Give the extent of all uninfected red blood cells.
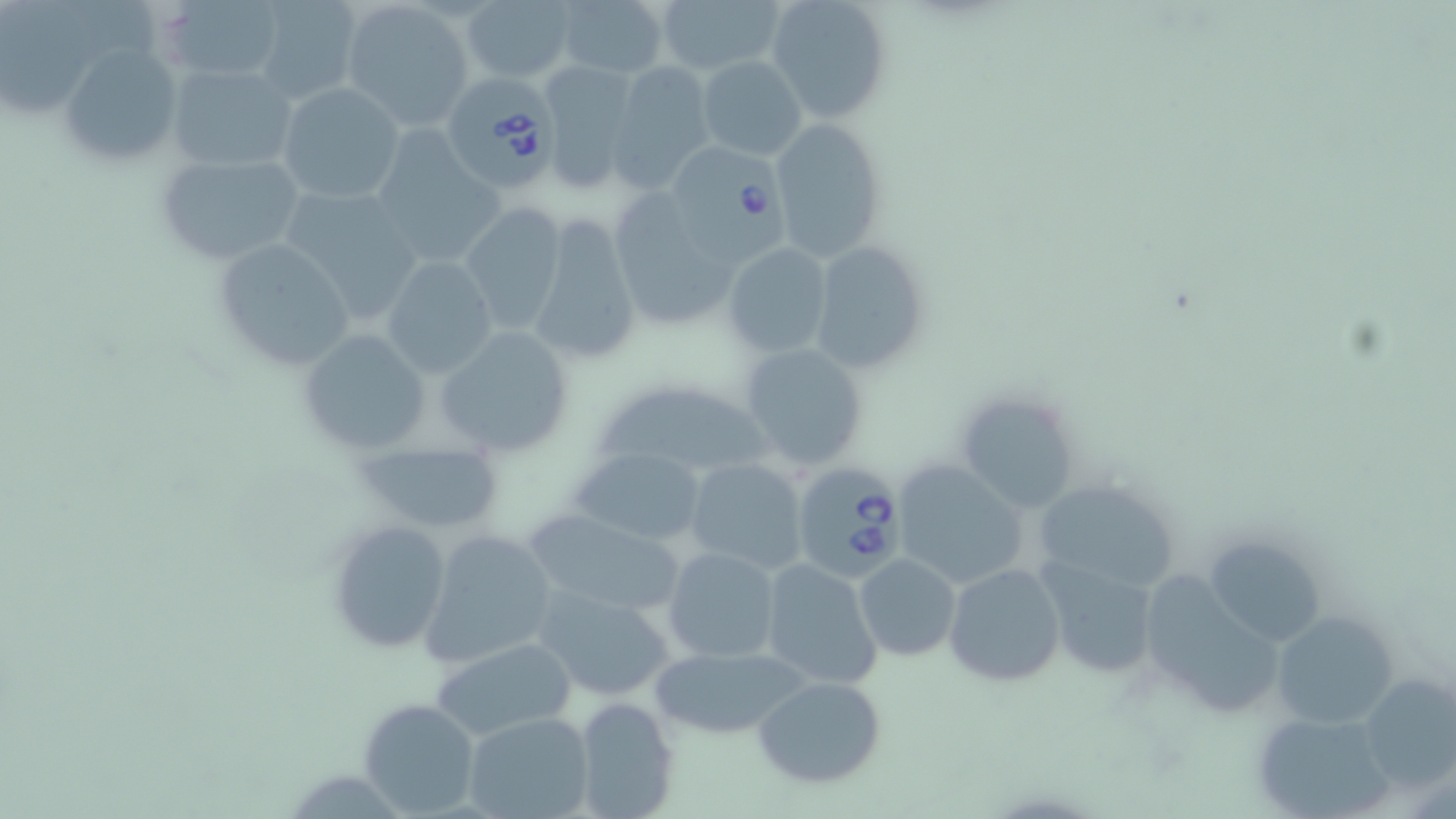

Approximate bounding boxes as (x1,y1)-(x2,y2) corner pairs in pixels.
Uninfected red blood cells: (160,0)-(284,85), (249,0)-(365,104), (556,0)-(669,79), (655,0)-(784,78), (765,0)-(892,124), (1,1)-(94,111), (344,1)-(475,129), (462,1)-(576,84), (60,44)-(182,168), (696,54)-(808,160), (610,61)-(715,187), (538,63)-(639,191), (166,64)-(298,172), (276,82)-(406,204), (770,116)-(889,262), (368,132)-(506,270), (152,150)-(307,268), (281,186)-(426,326), (621,193)-(735,325), (459,201)-(566,336), (526,212)-(643,368), (212,236)-(356,373), (722,242)-(834,359), (808,242)-(927,372), (381,255)-(498,377), (431,326)-(574,459), (296,327)-(431,456), (738,342)-(870,471), (589,377)-(774,487), (951,391)-(1082,515), (355,438)-(504,532), (571,447)-(711,547), (683,457)-(809,575), (891,458)-(1030,591), (1027,476)-(1183,595), (523,511)-(687,617), (325,517)-(451,654), (418,529)-(559,666), (1204,535)-(1326,651), (663,546)-(780,663), (854,553)-(960,661), (1037,557)-(1163,681), (758,558)-(883,692), (942,563)-(1066,686), (533,586)-(678,704), (1272,610)-(1399,730), (431,636)-(575,741), (647,644)-(809,740), (1358,672)-(1456,793), (754,676)-(885,788), (574,696)-(677,819), (358,697)-(481,816), (1253,710)-(1395,819), (464,712)-(593,819).

Summary:
  - Babesia divergens-infected red blood cell locations: (449,79)-(554,193), (675,143)-(787,272), (792,461)-(913,583)
  - Slide-level diagnosis: Babesia divergens
  - Modality: optical microscopy
  - Stain: May-Grünwald-Giemsa
  - Field of view: one of a larger specimen
  - Image size: 1456×819 pixels
  - Preparation: thin blood smear
  - Magnification: 1000x